Describe the morphology of the red blood cells.
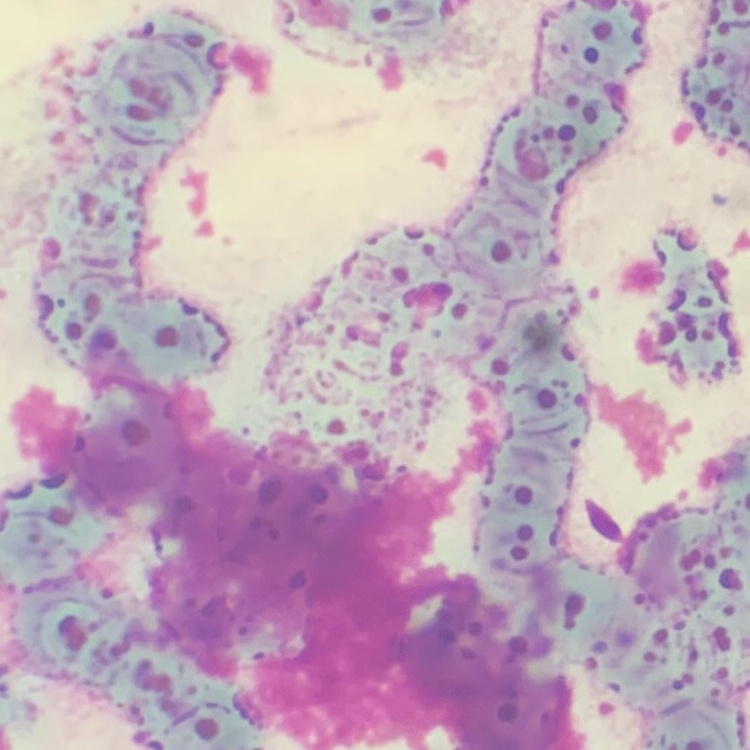
They show rouleaux formation.

Thin blood film. Field's or Giemsa stain. Square crop of a larger photomicrograph.